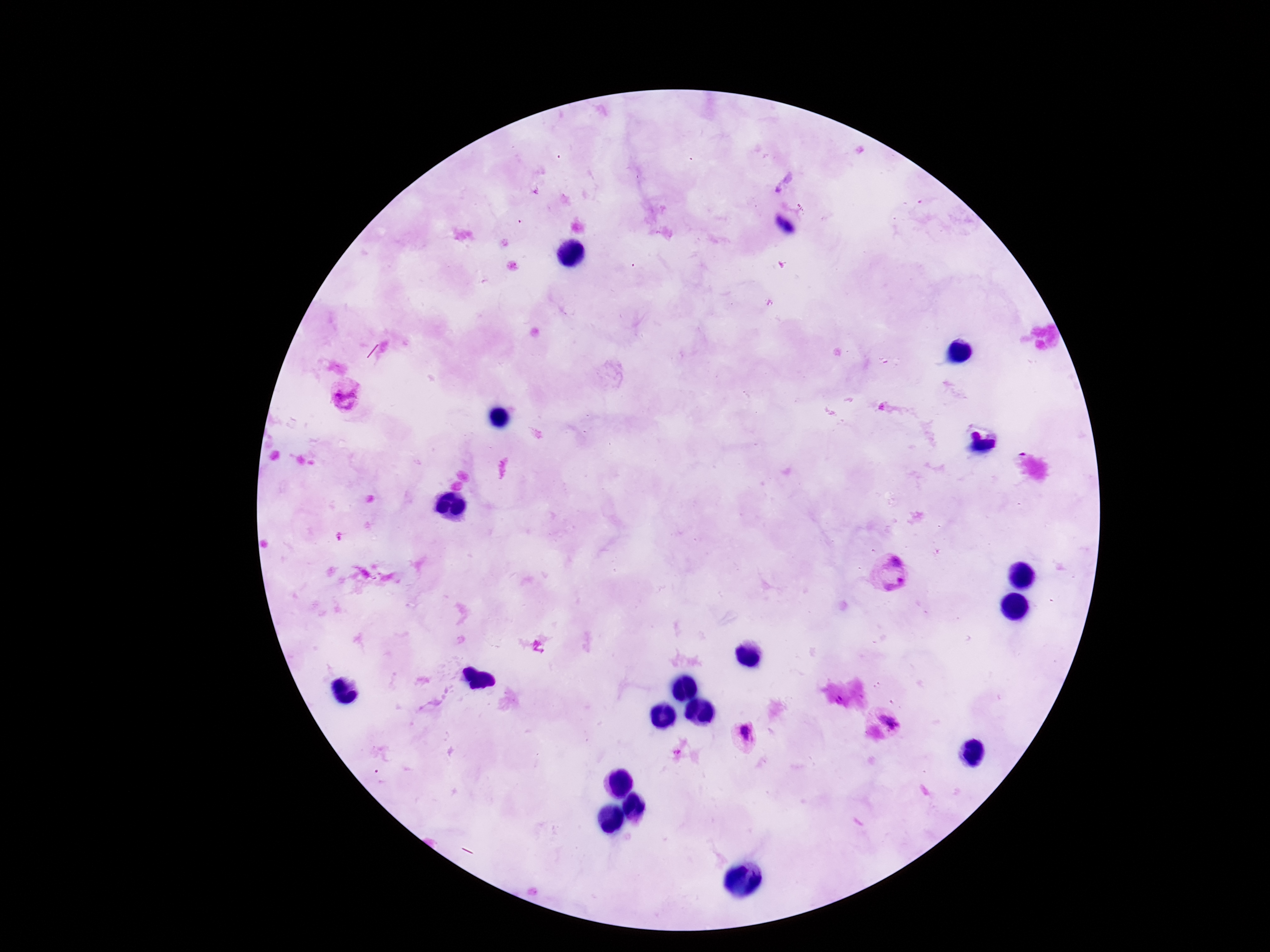 Approximate centers as {x, y} in pixels. Plasmodium parasite locations: {784, 182}, {344, 396}, {890, 573}, {890, 722}, {743, 735}. Giemsa-stained preparation. Patient malaria status: infected. 100x magnification. Image is 1270×952 pixels. Thick blood film. Single field of view. Smartphone photograph taken through the microscope eyepiece.